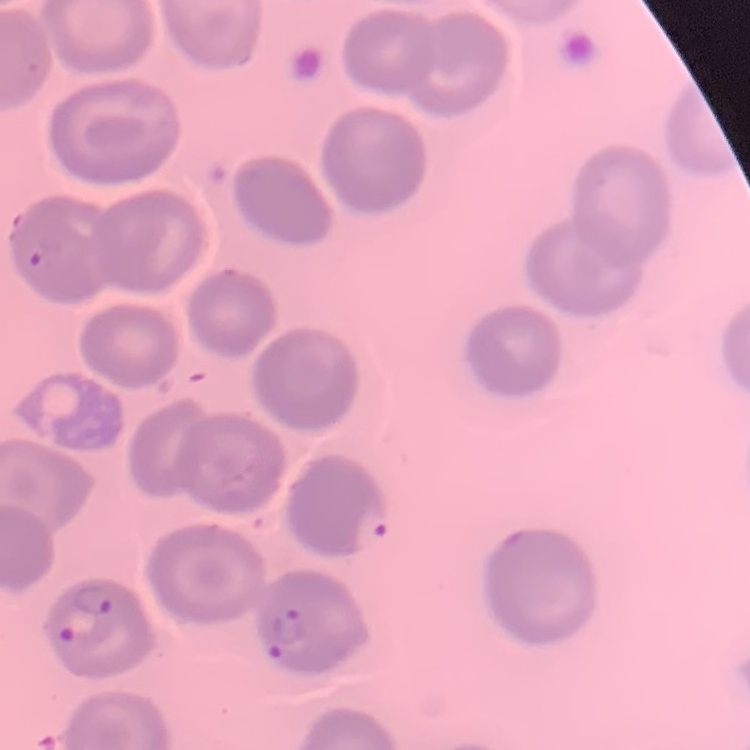
red blood cell morphology = no rouleaux formation
image type = square crop of a larger photomicrograph
preparation = thin blood film
stain = Field's or Giemsa